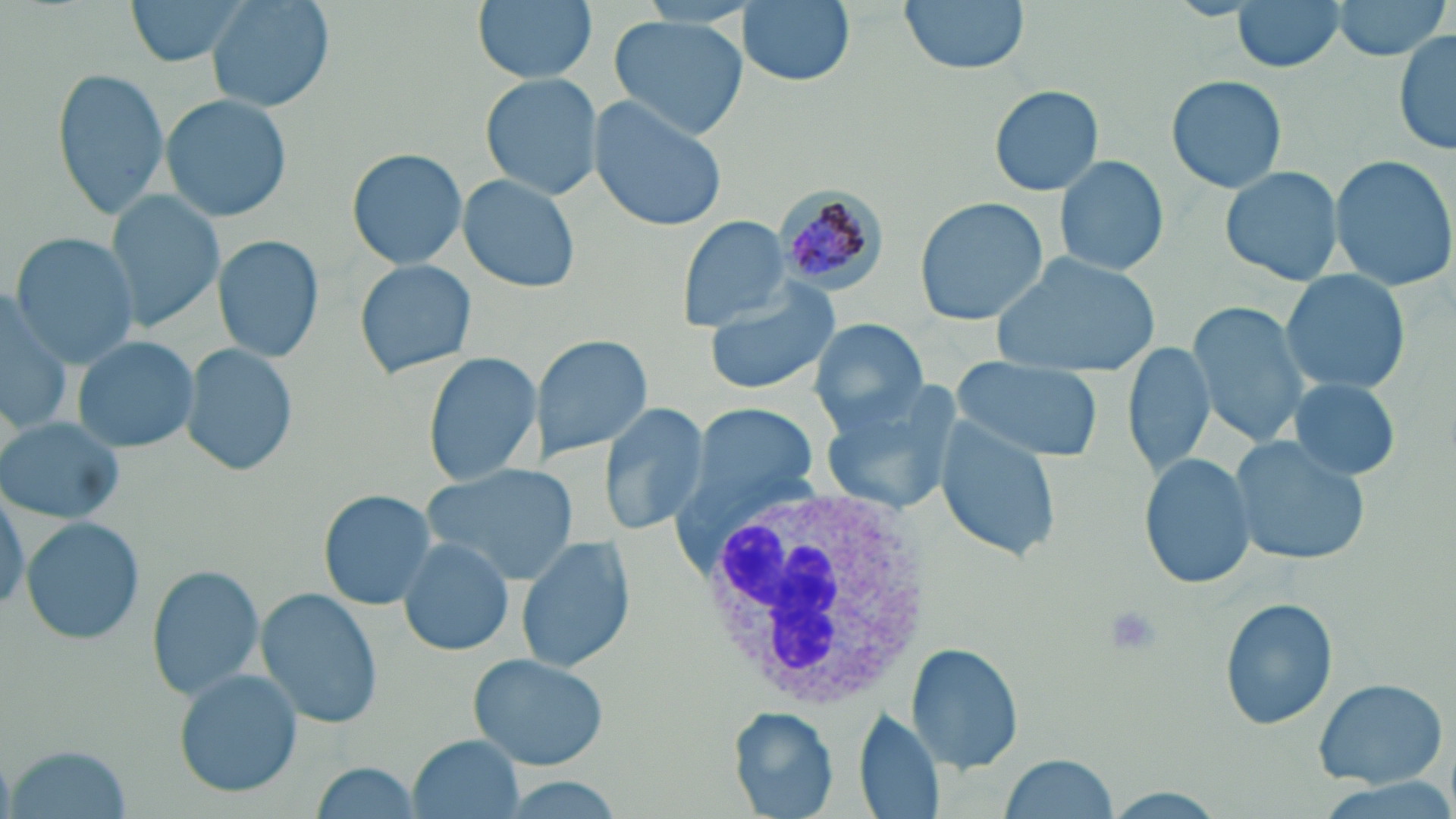 Approximate bounding boxes as named x1/y1/x2/y2 corners in pixels. Plasmodium malariae-infected red blood cell locations: (x1=772, y1=185, x2=887, y2=296). Platelet locations: (x1=1103, y1=607, x2=1162, y2=658). White blood cell locations: (x1=690, y1=484, x2=935, y2=714). Uninfected red blood cell locations: (x1=124, y1=0, x2=255, y2=66), (x1=209, y1=0, x2=333, y2=111), (x1=472, y1=0, x2=596, y2=84), (x1=738, y1=0, x2=856, y2=87), (x1=898, y1=0, x2=1028, y2=73), (x1=1230, y1=0, x2=1348, y2=72), (x1=1332, y1=0, x2=1451, y2=59), (x1=608, y1=14, x2=748, y2=141), (x1=1393, y1=29, x2=1456, y2=157), (x1=53, y1=66, x2=171, y2=222), (x1=479, y1=71, x2=600, y2=200), (x1=1167, y1=73, x2=1288, y2=193), (x1=990, y1=85, x2=1103, y2=196), (x1=161, y1=93, x2=296, y2=223), (x1=589, y1=94, x2=731, y2=233), (x1=347, y1=147, x2=469, y2=271), (x1=1052, y1=154, x2=1171, y2=278), (x1=1328, y1=154, x2=1456, y2=290), (x1=1220, y1=165, x2=1343, y2=285), (x1=458, y1=174, x2=583, y2=293), (x1=107, y1=189, x2=225, y2=332), (x1=914, y1=196, x2=1048, y2=326), (x1=676, y1=214, x2=792, y2=331), (x1=9, y1=232, x2=140, y2=368), (x1=214, y1=235, x2=325, y2=362), (x1=990, y1=251, x2=1161, y2=378), (x1=352, y1=258, x2=478, y2=380), (x1=1278, y1=268, x2=1411, y2=394), (x1=702, y1=282, x2=844, y2=395), (x1=0, y1=287, x2=74, y2=429), (x1=1186, y1=299, x2=1311, y2=445), (x1=809, y1=318, x2=929, y2=435), (x1=528, y1=332, x2=653, y2=464), (x1=72, y1=335, x2=199, y2=454), (x1=1122, y1=341, x2=1214, y2=478), (x1=182, y1=343, x2=298, y2=476), (x1=422, y1=350, x2=543, y2=486), (x1=952, y1=361, x2=1100, y2=462), (x1=1289, y1=377, x2=1401, y2=482), (x1=820, y1=385, x2=964, y2=515), (x1=598, y1=401, x2=711, y2=535), (x1=694, y1=403, x2=819, y2=512), (x1=934, y1=412, x2=1061, y2=562), (x1=0, y1=417, x2=125, y2=523), (x1=1228, y1=438, x2=1367, y2=566), (x1=1138, y1=453, x2=1256, y2=590), (x1=420, y1=465, x2=579, y2=584), (x1=0, y1=483, x2=28, y2=614), (x1=317, y1=489, x2=436, y2=609), (x1=21, y1=517, x2=145, y2=646), (x1=398, y1=537, x2=515, y2=656), (x1=514, y1=537, x2=636, y2=674), (x1=149, y1=565, x2=263, y2=699), (x1=256, y1=589, x2=384, y2=731), (x1=1220, y1=599, x2=1338, y2=731), (x1=906, y1=643, x2=1025, y2=774), (x1=467, y1=651, x2=611, y2=771), (x1=173, y1=669, x2=303, y2=797), (x1=1312, y1=677, x2=1450, y2=788), (x1=853, y1=706, x2=945, y2=816), (x1=725, y1=707, x2=838, y2=818), (x1=410, y1=734, x2=525, y2=818), (x1=7, y1=745, x2=136, y2=817), (x1=995, y1=754, x2=1122, y2=818), (x1=309, y1=762, x2=429, y2=818). Slide-level diagnosis: Plasmodium malariae. Captured at 1000x magnification. May-Grünwald-Giemsa stain. One field of a larger specimen. Optical microscopy. Image is 1456×819 pixels. Thin blood film.